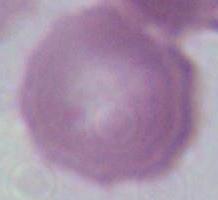

Summary:
  - Modality: photomicrograph
  - Magnification: 1000x
  - Identification: erythrocyte